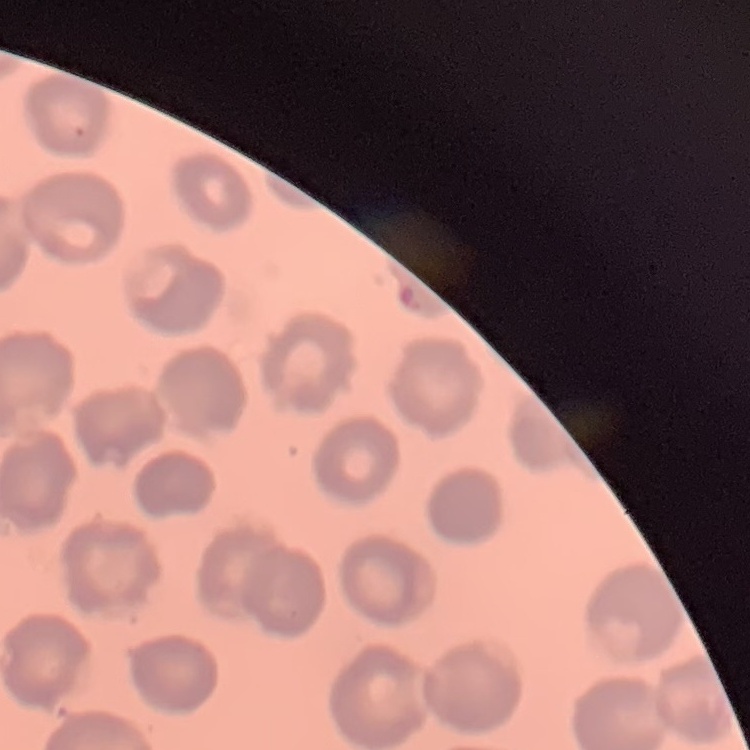

Summary:
  - Erythrocyte morphology: no rouleaux formation
  - Image type: one tile cut from a larger photomicrograph
  - Preparation: thin blood smear
  - Stain: Field's or Giemsa